Identify the parasite.
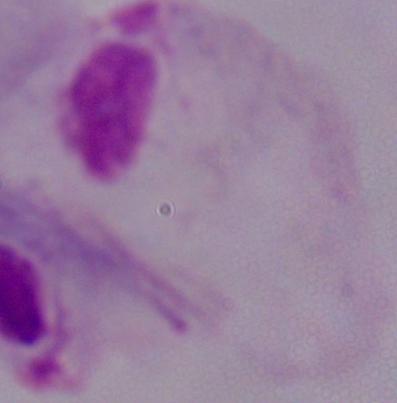

A trichomonad.

{
  "magnification": "1000x",
  "modality": "photomicrograph"
}